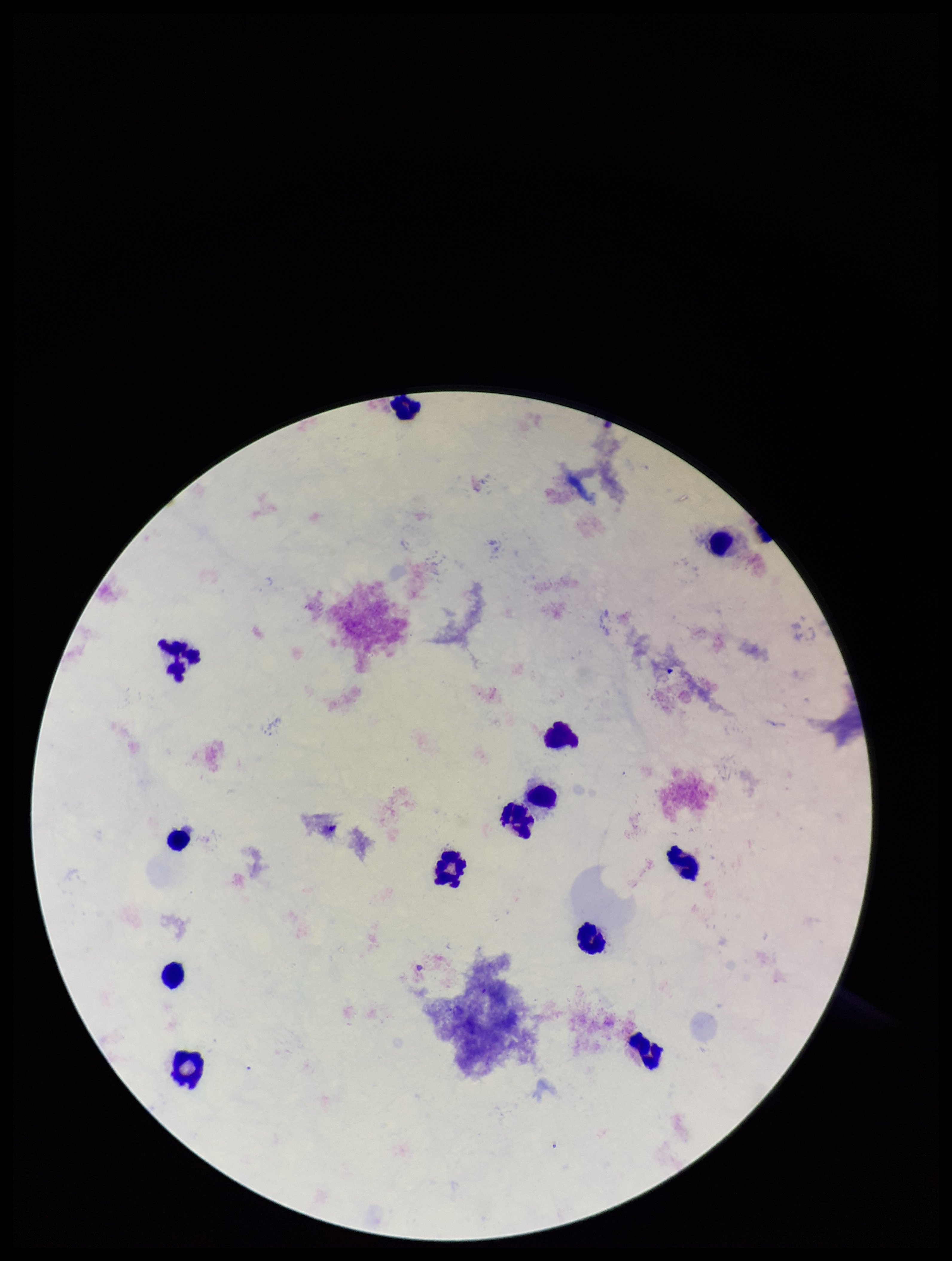

preparation: thick
plasmodium_parasites: none detected
leukocyte_count: 13
patient_malaria_status: negative
image_size: 952×1261 pixels
capture: smartphone photograph through the microscope eyepiece
parasite_count: 0
field_of_view: one from this slide
stain: Giemsa